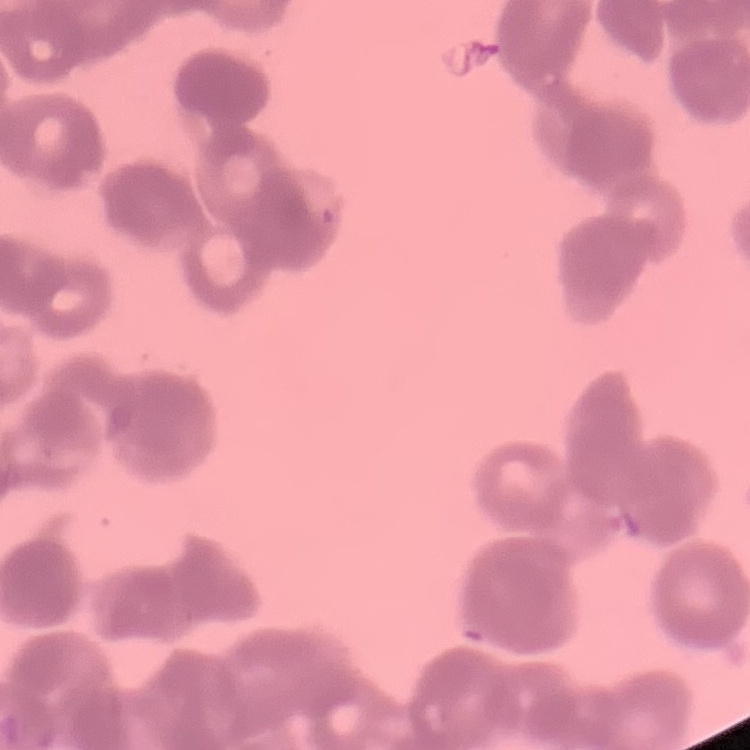
erythrocyte morphology = rouleaux formation
image type = one tile cut from a larger photomicrograph
stain = Field's or Giemsa
preparation = thin peripheral smear